Comment on the morphology of the red blood cells.
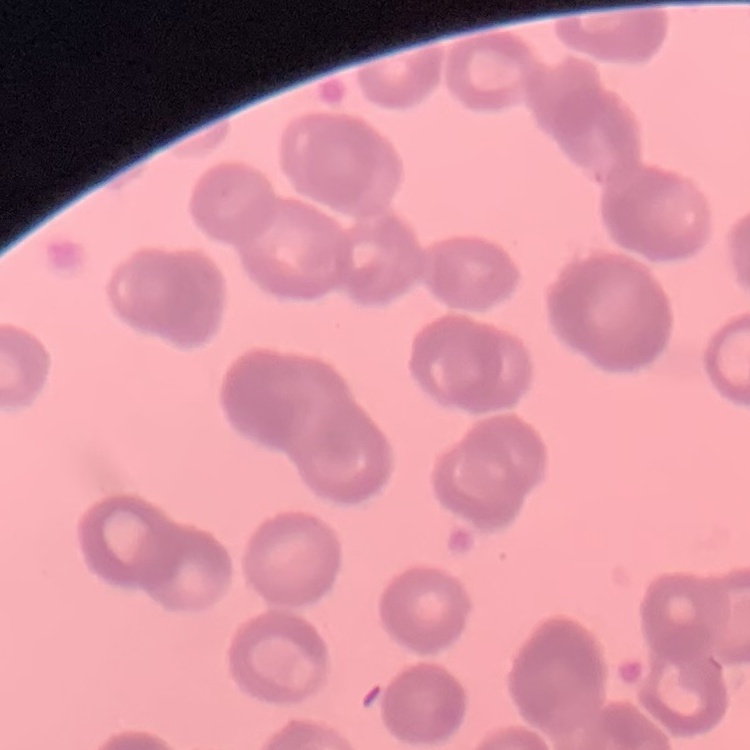
Rouleaux formation.

Square crop of a larger photomicrograph. Thin peripheral smear. Field's or Giemsa stain.